Locate every blood parasite and identify its species.
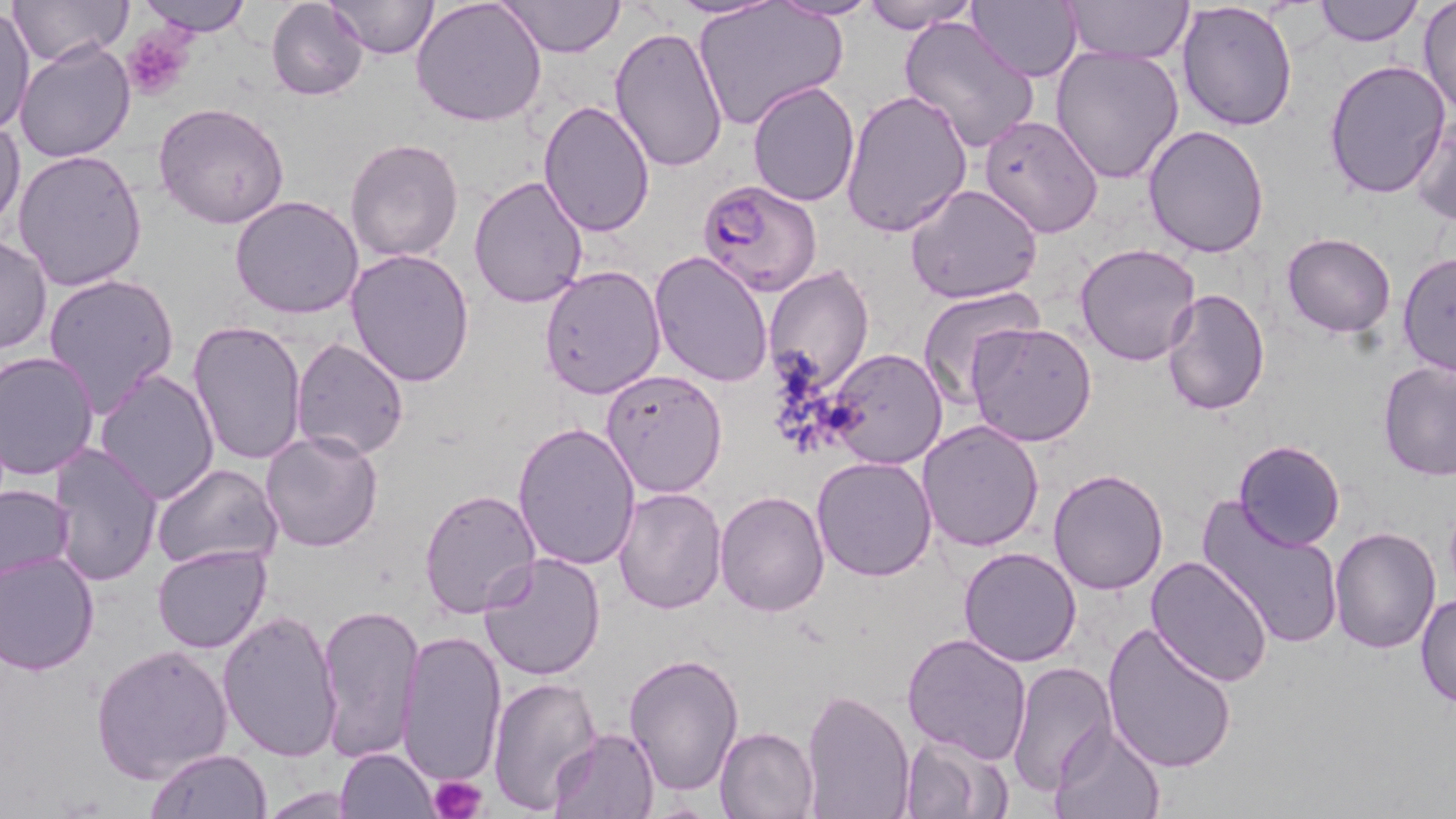
Approximate bounding boxes as [x1, y1, x2, y2] in pixels.
Plasmodium falciparum-infected red blood cells: [697, 178, 823, 295].
No Plasmodium ovale, Plasmodium malariae, Plasmodium vivax, Babesia divergens, or Trypanosoma brucei observed.

Summary:
  - Uninfected red blood cell locations: [8, 0, 131, 67], [135, 0, 252, 36], [265, 0, 368, 99], [325, 0, 439, 58], [412, 0, 548, 127], [502, 0, 622, 57], [667, 0, 781, 18], [769, 0, 876, 22], [861, 0, 981, 33], [968, 0, 1084, 83], [1063, 0, 1193, 62], [1312, 0, 1423, 46], [1177, 1, 1299, 132], [1417, 1, 1455, 117], [1, 3, 35, 137], [691, 3, 846, 131], [899, 15, 1040, 155], [608, 27, 730, 176], [13, 39, 136, 162], [1049, 43, 1185, 185], [1323, 58, 1453, 199], [748, 80, 862, 208], [838, 87, 971, 239], [539, 100, 655, 236], [154, 102, 291, 230], [1410, 109, 1456, 226], [978, 115, 1104, 239], [0, 116, 26, 229], [1142, 125, 1270, 258], [345, 136, 465, 264], [12, 149, 149, 292], [468, 174, 592, 309], [903, 182, 1044, 304], [231, 195, 366, 319], [1282, 232, 1396, 337], [0, 234, 51, 356], [1075, 244, 1203, 367], [345, 246, 476, 387], [648, 250, 775, 389], [1398, 251, 1455, 377], [539, 263, 667, 399], [762, 265, 876, 394], [43, 271, 180, 418], [915, 286, 1045, 409], [1161, 287, 1270, 415], [188, 321, 309, 470], [965, 321, 1097, 446], [290, 336, 410, 461], [0, 349, 99, 481], [822, 349, 947, 468], [1378, 360, 1456, 481], [93, 368, 219, 505], [600, 369, 729, 498], [915, 419, 1045, 554], [511, 420, 641, 572], [259, 428, 384, 553], [1232, 439, 1345, 550], [45, 440, 163, 585], [811, 455, 938, 582], [151, 461, 283, 571], [1047, 466, 1171, 595], [0, 480, 75, 585], [418, 486, 544, 617], [612, 486, 727, 613], [714, 489, 831, 616], [1197, 496, 1346, 652], [1329, 524, 1442, 651], [151, 543, 273, 654], [957, 546, 1084, 666], [1, 549, 101, 675], [476, 550, 606, 682], [1146, 555, 1274, 687], [1416, 592, 1456, 708], [316, 605, 426, 763], [218, 611, 344, 763], [1101, 619, 1237, 772], [397, 628, 505, 788], [901, 631, 1032, 762], [93, 644, 232, 782], [623, 654, 746, 795], [1008, 661, 1118, 797], [485, 674, 601, 816], [800, 689, 915, 819], [1047, 719, 1164, 819], [715, 726, 820, 818], [550, 728, 659, 817], [898, 733, 1014, 818], [335, 747, 439, 818], [147, 748, 273, 818], [255, 786, 366, 817]
  - Platelet locations: [121, 29, 196, 101], [428, 775, 489, 819]
  - Slide-level diagnosis: Plasmodium falciparum
  - Modality: optical microscopy
  - Stain: May-Grünwald-Giemsa
  - Field of view: one of a larger specimen
  - Magnification: 1000x
  - Image size: 1456×819 pixels
  - Preparation: thin blood smear